Outline each blood parasite and name the species.
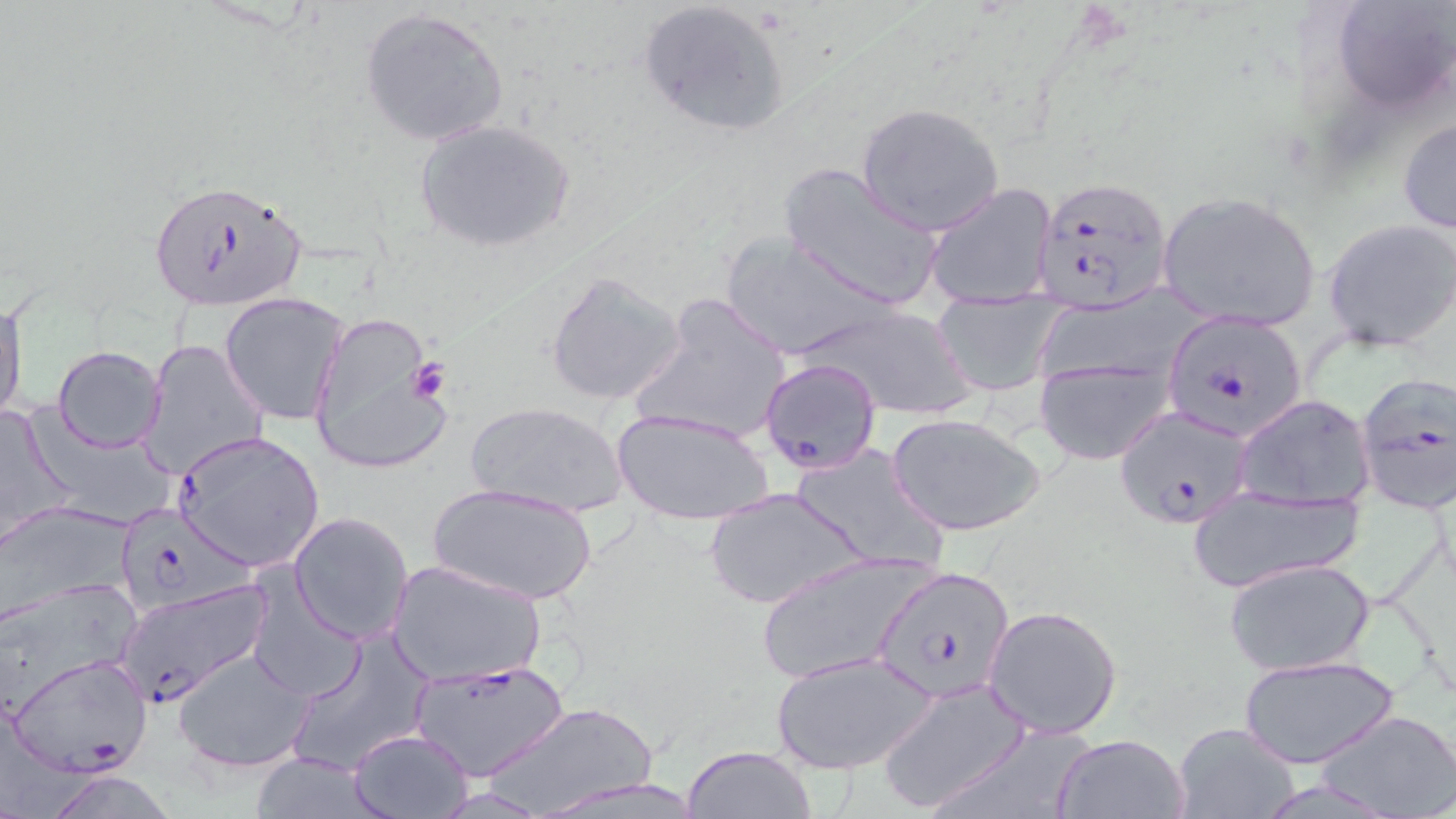
Approximate bounding boxes as (x1, y1, x2, y2) in pixels.
Plasmodium falciparum-infected red blood cells: (1030, 175, 1173, 312), (146, 178, 310, 314), (1164, 311, 1311, 443), (758, 358, 885, 478), (1353, 371, 1456, 513), (1115, 403, 1256, 529), (172, 431, 326, 572), (129, 509, 257, 615), (871, 565, 1014, 703), (117, 582, 271, 706), (9, 653, 153, 775), (410, 660, 570, 782).
No Plasmodium ovale, Plasmodium malariae, Plasmodium vivax, Babesia divergens, or Trypanosoma brucei observed.

Summary:
  - Platelet locations: (405, 356, 451, 404)
  - Uninfected red blood cell locations: (1333, 0, 1453, 114), (635, 1, 793, 136), (360, 6, 512, 148), (857, 103, 1003, 235), (1397, 114, 1456, 236), (414, 119, 577, 254), (777, 163, 946, 312), (923, 181, 1058, 305), (1155, 190, 1322, 332), (1323, 219, 1456, 352), (719, 233, 893, 359), (544, 270, 687, 407), (1028, 277, 1217, 397), (627, 293, 794, 448), (220, 294, 349, 425), (936, 296, 1060, 396), (0, 297, 26, 424), (798, 305, 975, 420), (309, 313, 446, 473), (140, 339, 269, 480), (52, 346, 166, 453), (1034, 357, 1174, 465), (1234, 394, 1375, 511), (464, 400, 630, 518), (1, 401, 79, 547), (35, 405, 180, 530), (612, 408, 775, 525), (889, 415, 1044, 536), (792, 442, 946, 574), (429, 484, 598, 607), (1188, 484, 1366, 591), (704, 487, 866, 611), (0, 503, 135, 622), (288, 512, 415, 646), (752, 549, 937, 685), (387, 558, 545, 687), (1224, 559, 1375, 676), (246, 571, 365, 702), (0, 579, 142, 718), (983, 604, 1123, 739), (283, 631, 434, 776), (173, 647, 312, 774), (771, 652, 936, 776), (1240, 654, 1398, 768), (877, 679, 1032, 813), (489, 701, 657, 817), (1316, 708, 1456, 818), (921, 721, 1099, 819), (1171, 721, 1302, 819), (346, 727, 474, 818), (1052, 732, 1190, 818), (682, 745, 816, 819), (244, 754, 393, 818), (533, 774, 712, 818)
  - Slide-level diagnosis: Plasmodium falciparum
  - Image size: 1456×819 pixels
  - Field of view: one of a larger specimen
  - Stain: May-Grünwald-Giemsa
  - Preparation: thin blood smear
  - Magnification: 1000x
  - Modality: optical microscopy